Name the blood parasite species.
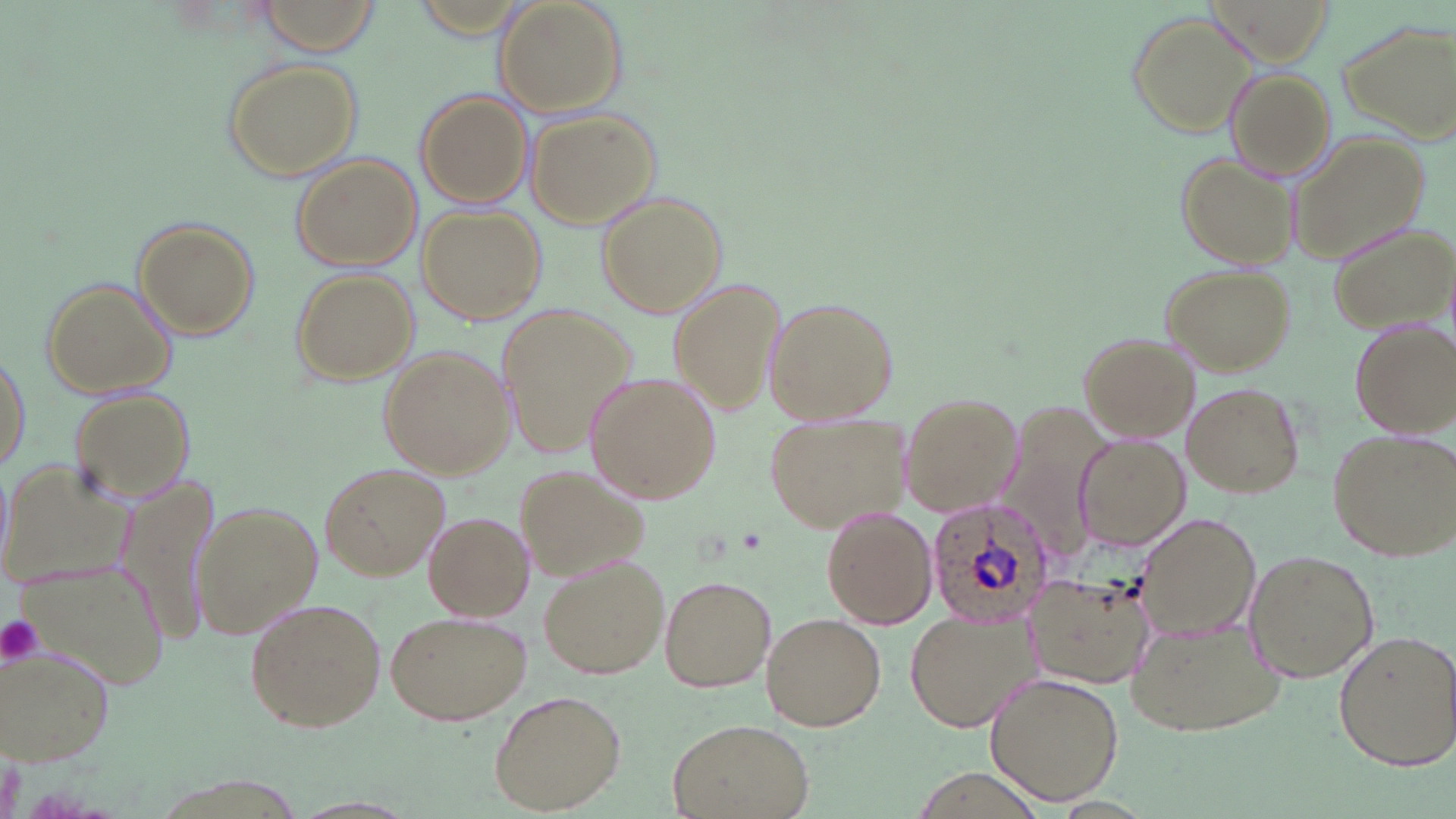

Plasmodium ovale.

Summary:
  - Coordinate format: approximate bounding boxes as (x1, y1, x2, y2) in pixels
  - Uninfected red blood cell locations: (257, 0, 382, 54), (493, 2, 625, 116), (1127, 9, 1257, 137), (1341, 17, 1455, 141), (222, 59, 365, 182), (1224, 69, 1336, 179), (415, 90, 533, 208), (526, 107, 662, 228), (1289, 131, 1431, 263), (1176, 152, 1299, 273), (292, 154, 422, 273), (596, 191, 726, 319), (420, 205, 548, 324), (131, 217, 259, 340), (1326, 220, 1455, 332), (1160, 264, 1292, 375), (291, 269, 417, 383), (40, 276, 180, 399), (668, 279, 787, 417), (762, 293, 899, 425), (497, 301, 637, 459), (1346, 317, 1455, 438), (1079, 332, 1201, 440), (378, 345, 516, 478), (0, 349, 31, 476), (583, 372, 721, 504), (1181, 381, 1305, 499), (68, 386, 198, 506), (902, 392, 1021, 518), (1012, 398, 1116, 559), (766, 409, 914, 533), (1326, 426, 1454, 561), (1077, 435, 1190, 549), (2, 457, 134, 589), (320, 462, 450, 581), (514, 463, 649, 577), (117, 471, 219, 643), (192, 499, 324, 642), (820, 504, 937, 628), (423, 511, 535, 621), (1136, 513, 1261, 642), (1243, 549, 1380, 684), (21, 552, 168, 690), (537, 553, 671, 679), (1023, 569, 1152, 688), (659, 574, 777, 692), (246, 597, 387, 733), (386, 609, 532, 725), (762, 612, 887, 731), (904, 612, 1039, 732), (1128, 616, 1285, 736), (1332, 629, 1454, 770), (3, 647, 116, 769), (983, 670, 1124, 806), (488, 691, 624, 814), (666, 716, 815, 819)
  - Platelet locations: (0, 613, 44, 667)
  - Plasmodium ovale-infected red blood cell locations: (924, 497, 1055, 629)
  - Preparation: thin blood smear
  - Image size: 1456×819 pixels
  - Modality: light microscopy
  - Stain: May-Grünwald-Giemsa
  - Magnification: 1000x
  - Field of view: single